Report the malaria status of this cell.
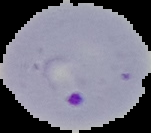

Parasitized.

Summary:
  - Preparation: thin blood smear
  - Image size: 151×133 pixels
  - Image type: segmented cell region with the area outside set to black